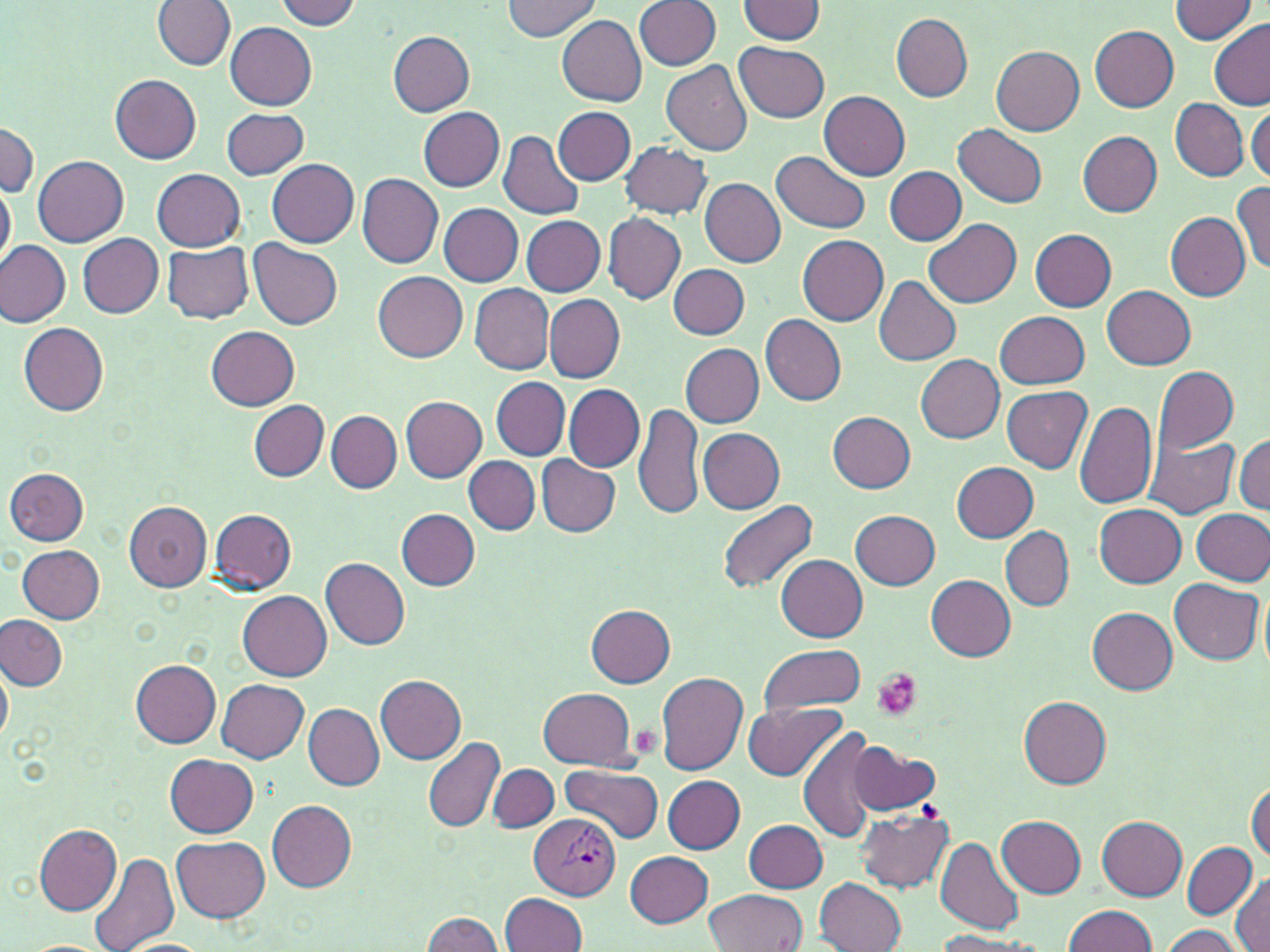
slide-level diagnosis = Plasmodium vivax
uninfected red blood cell locations = approximate bounding boxes as [x1, y1, x2, y2] in pixels: [503, 0, 601, 40], [1169, 0, 1258, 44], [153, 1, 235, 70], [273, 1, 365, 29], [633, 1, 719, 70], [737, 1, 827, 44], [891, 12, 972, 101], [556, 15, 647, 104], [1209, 20, 1270, 109], [226, 22, 316, 109], [1091, 25, 1179, 112], [389, 32, 476, 116], [735, 42, 829, 121], [992, 45, 1085, 136], [661, 58, 753, 156], [110, 74, 202, 163], [820, 90, 909, 180], [1170, 98, 1249, 181], [554, 106, 635, 185], [221, 107, 308, 180], [419, 107, 504, 192], [1247, 107, 1269, 184], [0, 119, 38, 200], [954, 124, 1048, 207], [498, 130, 585, 220], [1076, 130, 1161, 217], [621, 142, 710, 219], [772, 151, 870, 233], [33, 156, 129, 247], [267, 158, 359, 247], [884, 166, 967, 244], [153, 170, 245, 251], [357, 173, 444, 267], [699, 179, 785, 266], [0, 180, 15, 272], [1232, 182, 1270, 276], [438, 203, 524, 287], [1166, 211, 1250, 300], [604, 213, 685, 305], [521, 216, 606, 295], [925, 219, 1022, 307], [1030, 229, 1116, 310], [79, 234, 162, 318], [797, 235, 889, 326], [0, 238, 70, 327], [250, 238, 343, 327], [162, 242, 255, 324], [669, 264, 750, 339], [373, 271, 468, 360], [874, 275, 961, 366], [471, 284, 555, 373], [1103, 285, 1194, 369], [544, 293, 625, 383], [995, 310, 1089, 389], [760, 314, 846, 405], [19, 323, 108, 417], [205, 324, 299, 409], [681, 344, 764, 428], [916, 354, 1005, 443], [1152, 364, 1238, 454], [491, 377, 570, 460], [564, 385, 644, 472], [1002, 387, 1091, 472], [399, 396, 486, 482], [249, 400, 328, 482], [1074, 400, 1157, 508], [634, 402, 705, 522], [326, 410, 401, 493], [826, 411, 916, 492], [698, 427, 786, 513], [1144, 435, 1237, 519], [1234, 435, 1269, 514], [537, 455, 621, 537], [464, 456, 540, 534], [952, 462, 1038, 542], [5, 468, 90, 544], [11, 469, 95, 621], [717, 499, 819, 594], [124, 501, 212, 591], [1093, 503, 1187, 586], [397, 508, 479, 590], [1192, 508, 1270, 585], [209, 509, 298, 593], [851, 510, 939, 588], [1001, 527, 1073, 609], [16, 545, 104, 623], [775, 555, 868, 640], [321, 558, 410, 649], [926, 574, 1018, 658], [1170, 578, 1263, 665], [239, 592, 333, 680], [586, 605, 674, 686], [1087, 606, 1178, 692], [0, 615, 67, 692], [759, 644, 864, 715], [131, 659, 221, 748], [0, 663, 12, 745], [129, 668, 307, 753], [655, 673, 749, 774], [376, 675, 466, 764], [217, 679, 308, 763], [538, 688, 638, 769], [1019, 696, 1111, 788], [742, 703, 849, 782], [303, 704, 384, 790], [797, 726, 880, 843], [422, 736, 504, 834], [850, 744, 942, 816], [166, 755, 259, 837], [488, 764, 557, 832], [561, 764, 663, 843], [663, 776, 745, 852], [1246, 780, 1269, 863], [267, 800, 356, 892], [855, 809, 955, 894], [997, 816, 1085, 898], [1098, 817, 1188, 899], [743, 819, 828, 892], [33, 823, 121, 915], [171, 835, 270, 923], [936, 838, 1023, 935], [1181, 841, 1256, 919], [88, 846, 181, 952], [626, 851, 713, 927], [1231, 873, 1270, 952], [816, 876, 907, 952], [702, 890, 807, 952], [500, 892, 587, 951], [1063, 905, 1159, 952], [422, 911, 505, 952], [1157, 925, 1247, 951], [931, 930, 1048, 951]
modality = light microscopy
stain = May-Grünwald-Giemsa
magnification = 1000x
image size = 1270×952 pixels
Plasmodium vivax-infected red blood cell locations = approximate bounding boxes as [x1, y1, x2, y2] in pixels: [531, 812, 621, 899]
field of view = single
platelet locations = approximate bounding boxes as [x1, y1, x2, y2] in pixels: [873, 669, 923, 721], [625, 724, 662, 759]
preparation = thin blood film